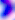

modality = micrograph
magnification = 400x
identification = Toxoplasma gondii